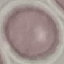

Summary:
  - Malaria status: uninfected
  - Capture: smartphone through the microscope eyepiece
  - Stain: Giemsa
  - Image type: automatically extracted cell patch, resized to 64 × 64 pixels
  - Preparation: thin blood film